Report the malaria status of this cell.
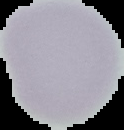
It is uninfected.

{
  "image_size": "124×130 pixels",
  "image_type": "cell region segmented out of the field of view; surrounding area masked to black",
  "preparation": "thin blood smear"
}